Report the malaria status of this cell.
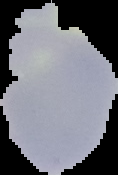
Uninfected.

Summary:
  - Preparation: thin blood smear
  - Image size: 118×175 pixels
  - Image type: cell region segmented out of the field of view; surrounding area masked to black